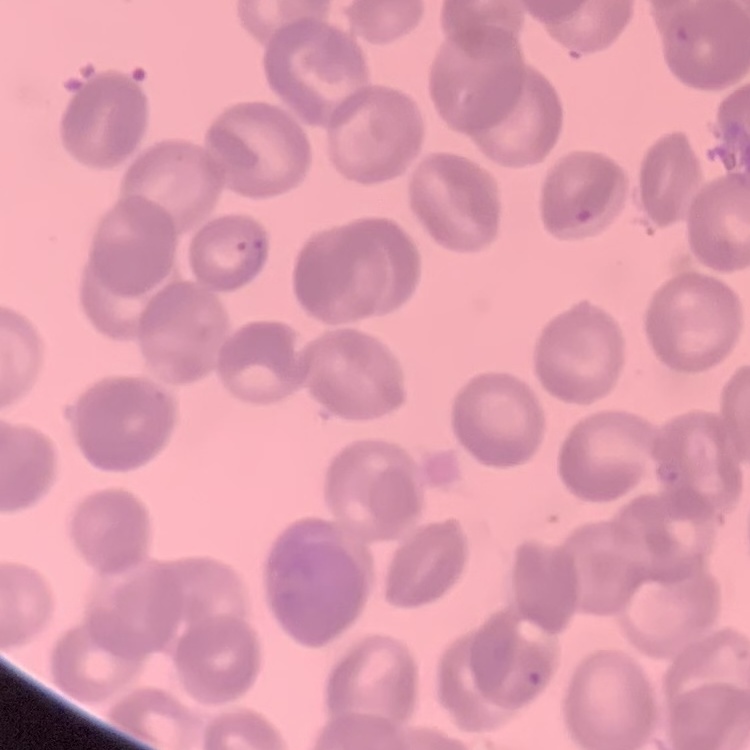
{
  "red_blood_cell_morphology": "rouleaux formation",
  "stain": "Field's or Giemsa",
  "preparation": "thin peripheral smear",
  "image_type": "square crop of a larger photomicrograph"
}